Comment on the morphology of the red blood cells.
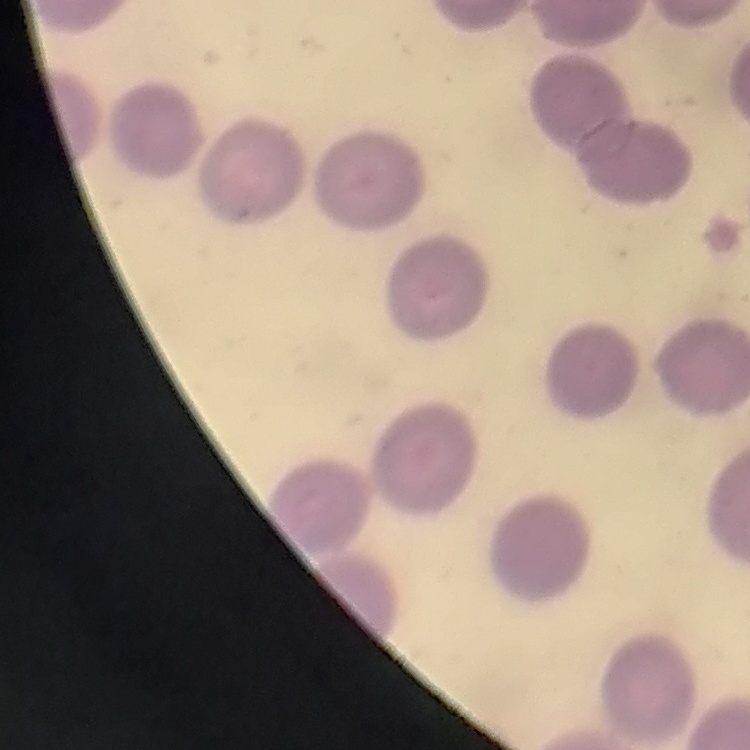

They show no rouleaux formation.

stain = Field's or Giemsa
image type = square crop of a larger photomicrograph
preparation = thin peripheral smear